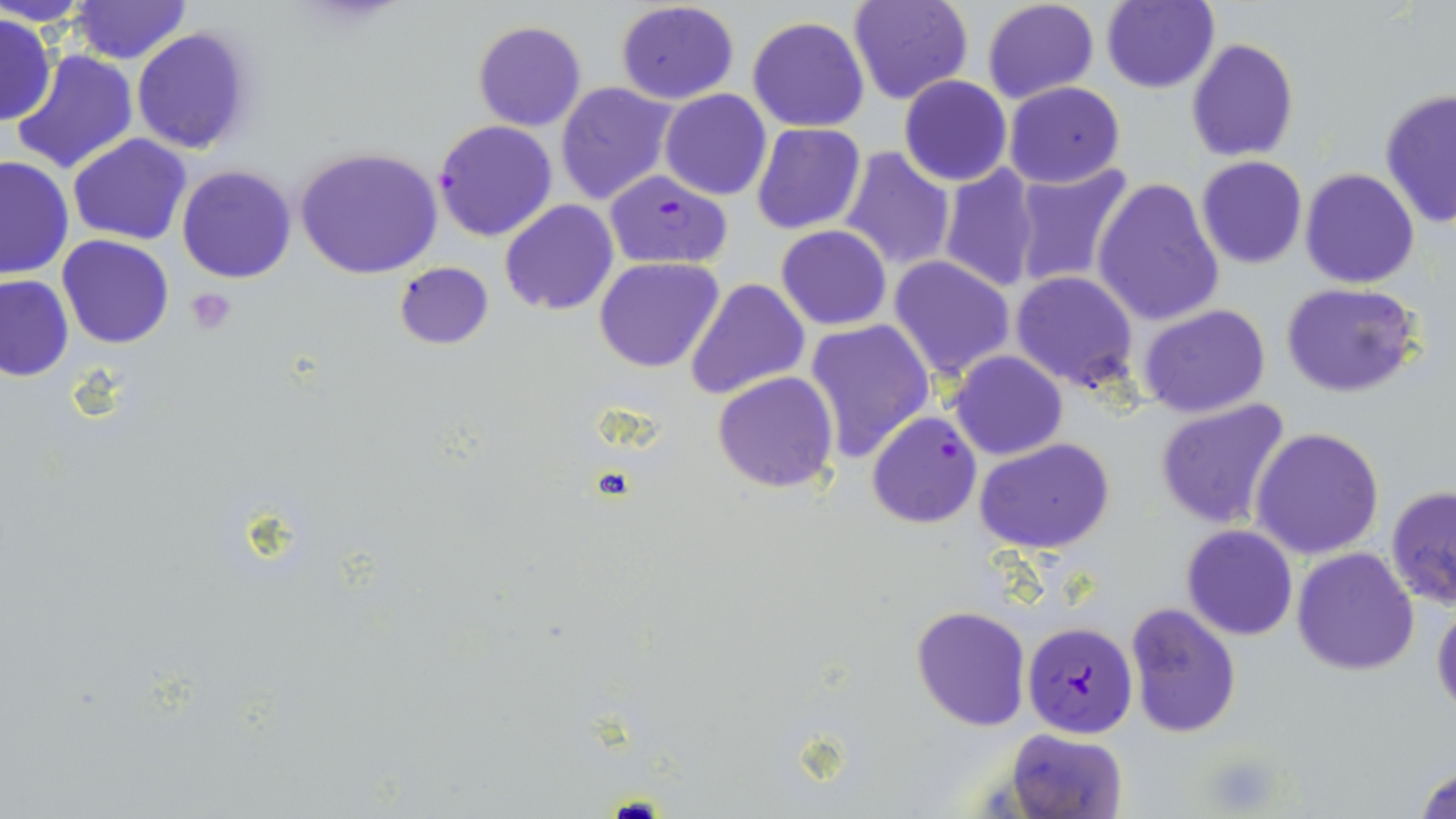
Approximate bounding boxes as named x1/y1/x2/y2 corners in pixels. Uninfected red blood cell locations: (x1=1, y1=0, x2=98, y2=27), (x1=70, y1=0, x2=190, y2=64), (x1=847, y1=0, x2=975, y2=106), (x1=981, y1=0, x2=1102, y2=105), (x1=615, y1=1, x2=739, y2=104), (x1=1099, y1=1, x2=1219, y2=94), (x1=0, y1=14, x2=56, y2=124), (x1=747, y1=14, x2=870, y2=132), (x1=471, y1=20, x2=588, y2=132), (x1=130, y1=26, x2=254, y2=156), (x1=1186, y1=36, x2=1298, y2=162), (x1=10, y1=48, x2=138, y2=176), (x1=898, y1=74, x2=1012, y2=187), (x1=1002, y1=81, x2=1126, y2=188), (x1=555, y1=82, x2=677, y2=207), (x1=660, y1=89, x2=771, y2=201), (x1=1379, y1=89, x2=1456, y2=231), (x1=752, y1=123, x2=866, y2=234), (x1=67, y1=134, x2=190, y2=245), (x1=295, y1=147, x2=444, y2=281), (x1=840, y1=147, x2=956, y2=270), (x1=0, y1=155, x2=76, y2=279), (x1=1195, y1=156, x2=1308, y2=269), (x1=937, y1=163, x2=1043, y2=295), (x1=1009, y1=163, x2=1137, y2=291), (x1=176, y1=166, x2=297, y2=284), (x1=1298, y1=167, x2=1421, y2=289), (x1=1092, y1=178, x2=1225, y2=328), (x1=499, y1=200, x2=618, y2=315), (x1=775, y1=226, x2=893, y2=330), (x1=58, y1=235, x2=174, y2=349), (x1=888, y1=256, x2=1016, y2=381), (x1=595, y1=257, x2=724, y2=374), (x1=393, y1=261, x2=493, y2=350), (x1=1011, y1=270, x2=1138, y2=393), (x1=0, y1=274, x2=73, y2=381), (x1=686, y1=277, x2=809, y2=400), (x1=1279, y1=280, x2=1424, y2=398), (x1=1137, y1=303, x2=1272, y2=420), (x1=804, y1=319, x2=935, y2=463), (x1=949, y1=351, x2=1067, y2=460), (x1=712, y1=372, x2=839, y2=493), (x1=1154, y1=400, x2=1293, y2=530), (x1=1252, y1=427, x2=1386, y2=560), (x1=974, y1=437, x2=1116, y2=554), (x1=1385, y1=485, x2=1456, y2=611), (x1=1181, y1=525, x2=1299, y2=641), (x1=1292, y1=547, x2=1419, y2=677), (x1=1432, y1=595, x2=1456, y2=717), (x1=1123, y1=603, x2=1243, y2=739), (x1=910, y1=605, x2=1031, y2=731), (x1=1006, y1=728, x2=1129, y2=819), (x1=1413, y1=761, x2=1456, y2=819). Plasmodium falciparum-infected red blood cell locations: (x1=433, y1=119, x2=559, y2=241), (x1=604, y1=171, x2=732, y2=270), (x1=866, y1=411, x2=981, y2=528), (x1=1021, y1=620, x2=1139, y2=738). Platelet locations: (x1=186, y1=288, x2=237, y2=335), (x1=1208, y1=754, x2=1283, y2=814). Slide-level diagnosis: Plasmodium falciparum. May-Grünwald-Giemsa-stained preparation. One field of a larger specimen. Image is 1456×819 pixels. Captured at 1000x magnification. Thin blood smear. Optical microscopy.